Classify this cell by malaria status.
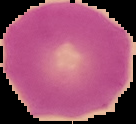

Uninfected.

The area outside the segmented cell region is set to black. Image is 136×124 pixels. From a thin blood smear.